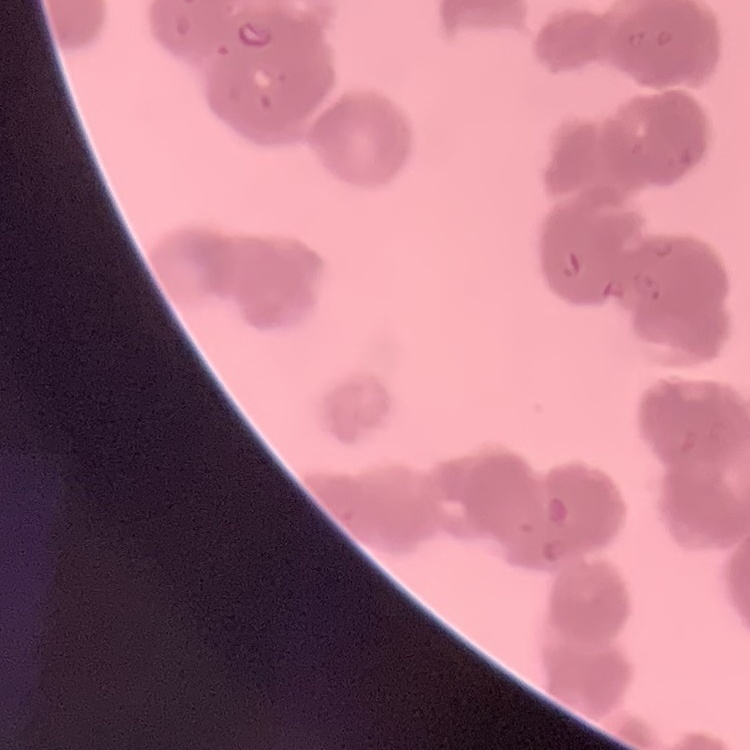 The red blood cells show rouleaux formation. Thin blood film. One tile cut from a larger photomicrograph. Stained with either Field's or Giemsa.